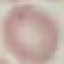
Summary:
  - Malaria status: uninfected
  - Stain: Giemsa
  - Image type: automatically extracted cell patch, resized to 64 × 64 pixels
  - Preparation: thin smear
  - Capture: smartphone camera at the microscope eyepiece